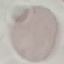
malaria status = uninfected
preparation = thin blood smear
capture = smartphone camera at the microscope eyepiece
image type = automatically extracted cell patch, resized to 64 × 64 pixels
stain = Giemsa